Report the malaria status of this cell.
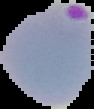
Parasitized.

image type = segmented cell region on a black background
preparation = thin blood film
image size = 94×109 pixels